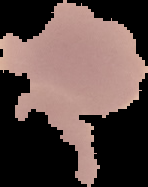
Cell region segmented out of the field of view; the surrounding area is masked to black. Image is 148×187 pixels. Result: no malaria parasites detected. From a thin blood film.